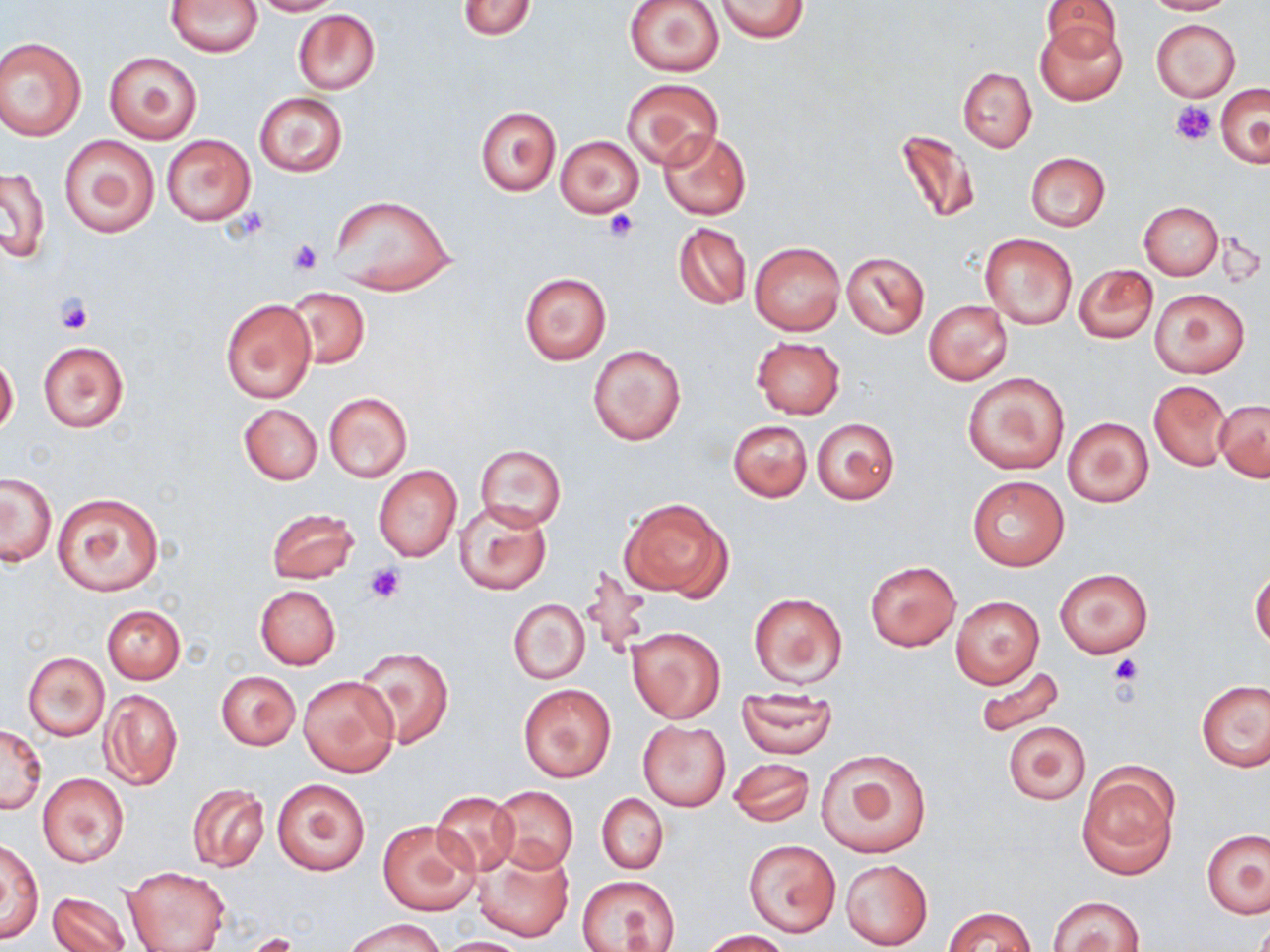

Approximate bounding boxes as (x1, y1, x2, y2) in pixels. Uninfected red blood cell locations: (167, 0, 263, 55), (251, 0, 337, 15), (715, 0, 809, 41), (1142, 0, 1233, 15), (458, 1, 536, 39), (624, 1, 725, 76), (1041, 1, 1124, 58), (292, 10, 381, 95), (1037, 18, 1126, 106), (1150, 19, 1240, 101), (0, 37, 86, 141), (104, 52, 202, 143), (957, 67, 1036, 152), (622, 79, 722, 169), (1216, 84, 1269, 167), (254, 92, 348, 177), (476, 106, 560, 196), (896, 128, 981, 224), (657, 130, 751, 220), (59, 133, 159, 239), (162, 133, 257, 226), (556, 135, 643, 218), (1025, 152, 1110, 230), (1, 166, 50, 264), (328, 195, 456, 296), (1138, 202, 1222, 280), (672, 222, 751, 310), (980, 234, 1077, 329), (749, 241, 845, 336), (842, 251, 929, 338), (1074, 264, 1158, 343), (518, 272, 613, 365), (287, 288, 370, 369), (1148, 288, 1249, 378), (221, 298, 316, 402), (923, 300, 1012, 386), (751, 336, 845, 419), (38, 340, 128, 433), (588, 344, 686, 445), (0, 352, 19, 438), (962, 372, 1070, 475), (1148, 380, 1231, 470), (324, 392, 413, 482), (1215, 400, 1269, 480), (239, 404, 322, 484), (1062, 417, 1152, 508), (812, 418, 899, 506), (728, 419, 811, 503), (474, 445, 566, 532), (373, 463, 461, 562), (1, 474, 56, 565), (967, 475, 1068, 570), (53, 491, 164, 597), (618, 494, 731, 601), (453, 501, 552, 595), (266, 507, 359, 583), (864, 560, 961, 652), (578, 562, 651, 661), (1054, 568, 1153, 658), (1251, 570, 1270, 649), (254, 586, 340, 669), (748, 591, 848, 688), (950, 595, 1044, 689), (509, 597, 590, 684), (101, 604, 185, 684), (625, 625, 726, 723), (354, 647, 455, 748), (24, 653, 109, 740), (976, 665, 1067, 740), (216, 670, 299, 749), (298, 675, 399, 777), (1196, 680, 1269, 772), (518, 682, 617, 784), (98, 688, 183, 791), (736, 688, 839, 758), (638, 721, 730, 810), (1003, 722, 1089, 804), (0, 724, 46, 814), (816, 748, 932, 858), (726, 757, 815, 827), (1078, 766, 1179, 881), (37, 773, 128, 867), (272, 777, 371, 876), (187, 783, 269, 873), (490, 785, 579, 873), (431, 790, 521, 875), (592, 793, 673, 952), (596, 793, 667, 873), (379, 820, 481, 915), (1202, 829, 1269, 918), (2, 838, 43, 945), (745, 840, 841, 936), (470, 846, 573, 942), (841, 859, 932, 949), (122, 866, 230, 952), (576, 874, 680, 951), (46, 890, 133, 952), (1047, 895, 1145, 952), (943, 906, 1036, 952), (344, 917, 444, 952), (702, 930, 791, 952), (434, 936, 536, 951). Platelet locations: (1172, 102, 1217, 144), (229, 208, 270, 243), (603, 209, 640, 243), (288, 238, 323, 275), (57, 295, 93, 335), (364, 562, 406, 602), (1108, 653, 1144, 686). Slide-level diagnosis: no evidence of blood parasites. Optical microscopy. Thin blood smear. Image is 1270×952 pixels. May-Grünwald-Giemsa stain. 1000x magnification. One field of a larger specimen.